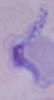

Summary:
  - Magnification: 1000x
  - Identification: trypanosome
  - Modality: photomicrograph